Assess this cell for malaria.
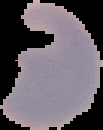

It is parasitized.

preparation = thin blood film
image type = segmented cell region on a black background
image size = 103×130 pixels